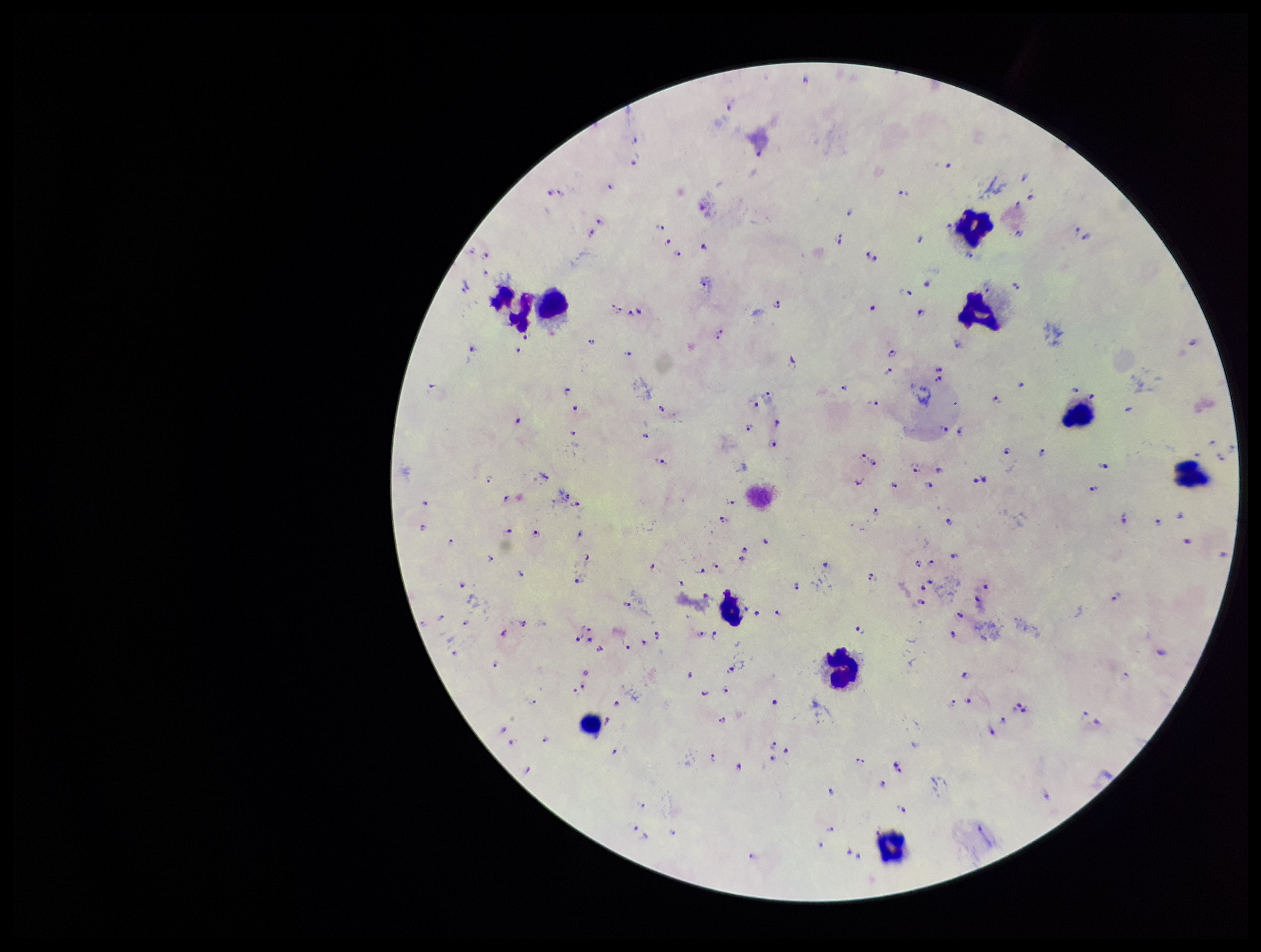

image size = 1261×952 pixels
field of view = single
Plasmodium parasites = seen
parasite count = 152
species reported for this patient = Plasmodium falciparum
leukocyte count = 10
preparation = thick smear
patient malaria status = infected
stain = Giemsa
capture = smartphone photograph through the microscope eyepiece